Comment on the morphology of the red blood cells.
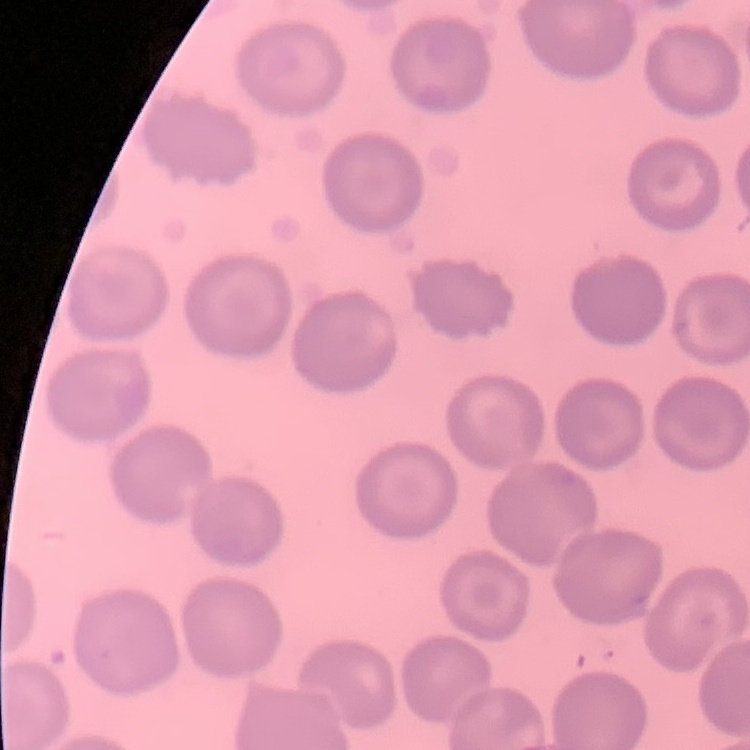

No rouleaux formation.

One tile cut from a larger photomicrograph. Thin peripheral smear. Field's or Giemsa stain.